State which parasite is depicted.
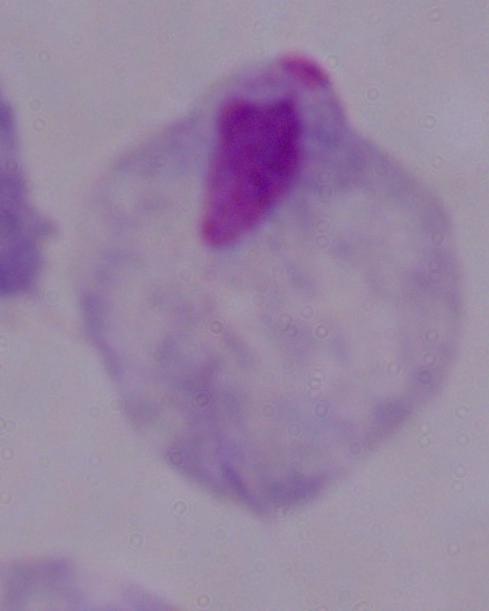

A trichomonad.

1000x magnification. Photomicrograph.